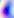
Summary:
  - Modality: micrograph
  - Magnification: 400x
  - Identification: Toxoplasma gondii